Assess the morphology of the erythrocytes.
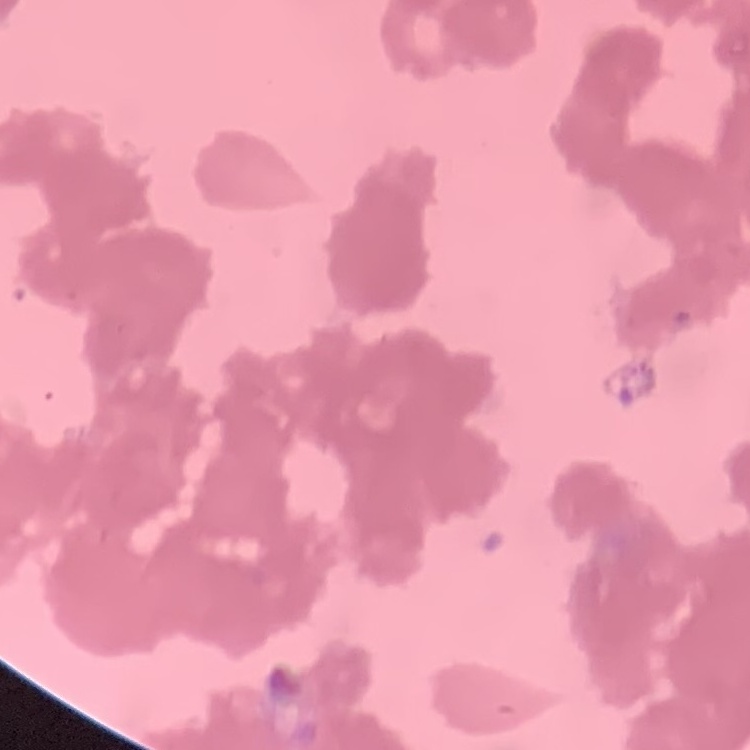

They show rouleaux formation.

stain = Field's or Giemsa
image type = square crop of a larger photomicrograph
preparation = thin peripheral smear